Describe the morphology of the erythrocytes.
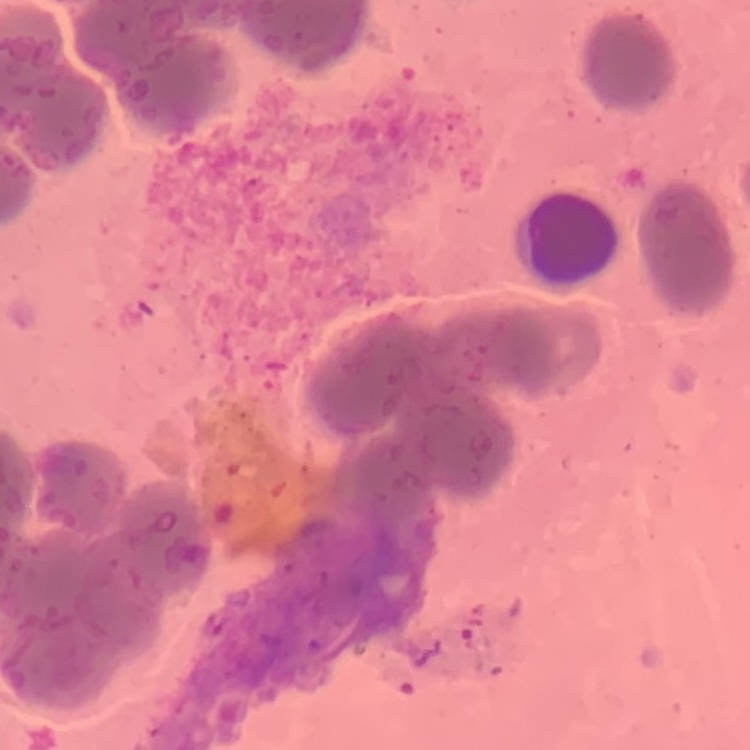
They show rouleaux formation.

Summary:
  - Stain: Field's or Giemsa
  - Preparation: thin peripheral smear
  - Image type: square crop of a larger photomicrograph